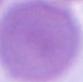

Micrograph. A red blood cell is shown. 1000x magnification.